Point out each leukocyte.
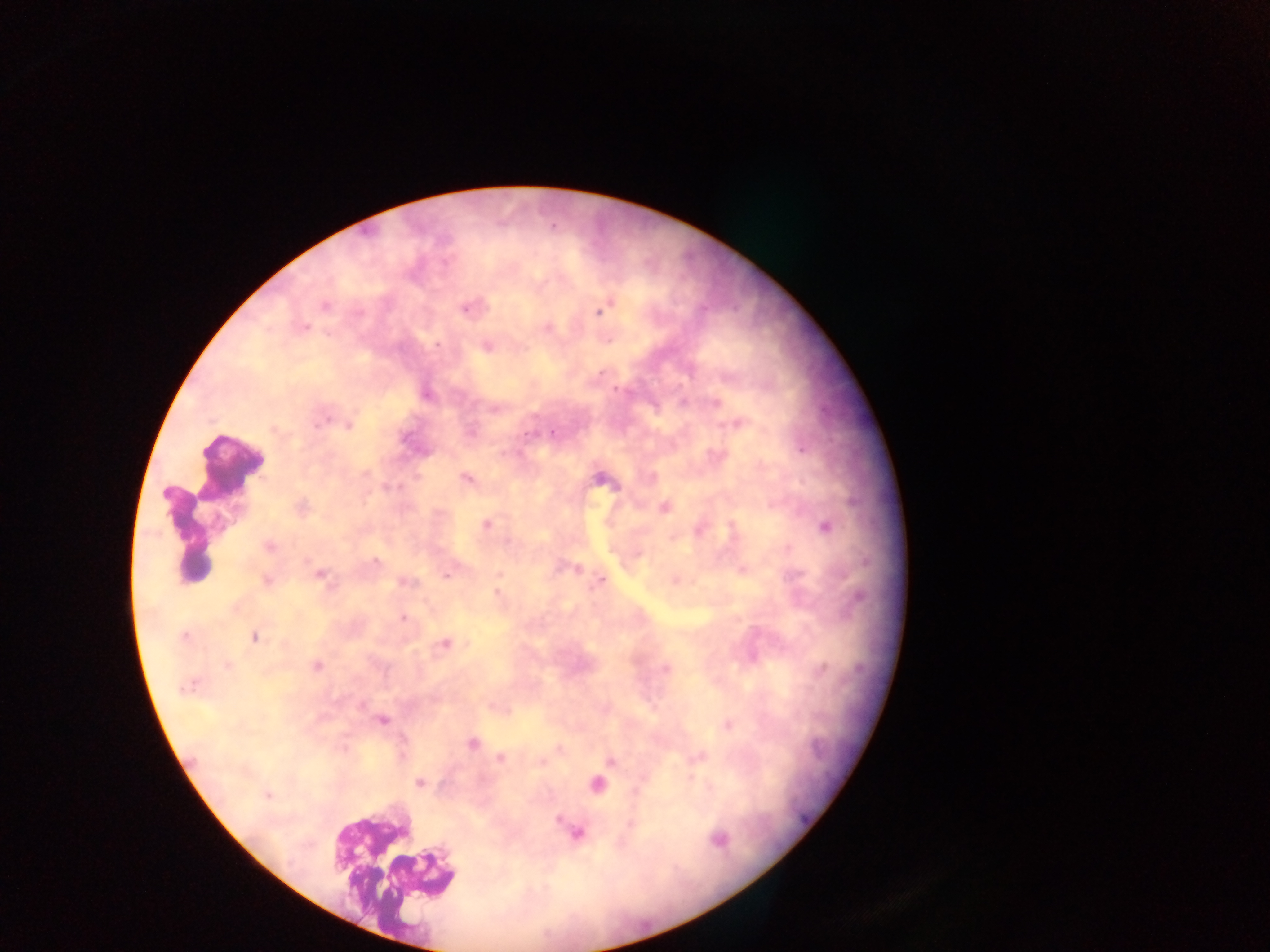

Approximate centers as (x, y) in pixels.
Leukocytes: (230, 463), (185, 535), (391, 862).

Plasmodium parasite locations: (324, 307), (466, 308), (600, 310), (304, 327), (548, 327), (437, 345), (487, 347), (427, 394), (318, 422), (738, 424), (348, 426), (274, 429), (553, 433), (466, 478), (602, 480), (301, 507), (665, 507), (486, 524), (825, 526), (269, 547), (374, 561), (578, 569), (320, 574), (446, 577), (266, 580), (602, 580), (405, 582), (497, 592), (403, 619), (184, 636), (255, 636), (445, 643), (227, 666), (317, 666), (667, 668), (822, 668), (186, 688), (361, 706), (383, 720), (727, 725), (472, 744), (401, 756), (500, 759), (612, 762), (418, 783), (268, 795), (718, 839). One field of view. Mobile-phone photograph taken through the microscope. Sample from Ghana. Image is 1270×952 pixels. Thick blood smear.